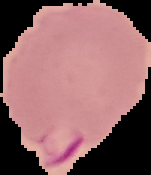

Cell region segmented out of the field of view; the surrounding area is masked to black. From a thin blood smear. Malaria status: parasitized. Image is 151×175 pixels.